Give the preparation type.
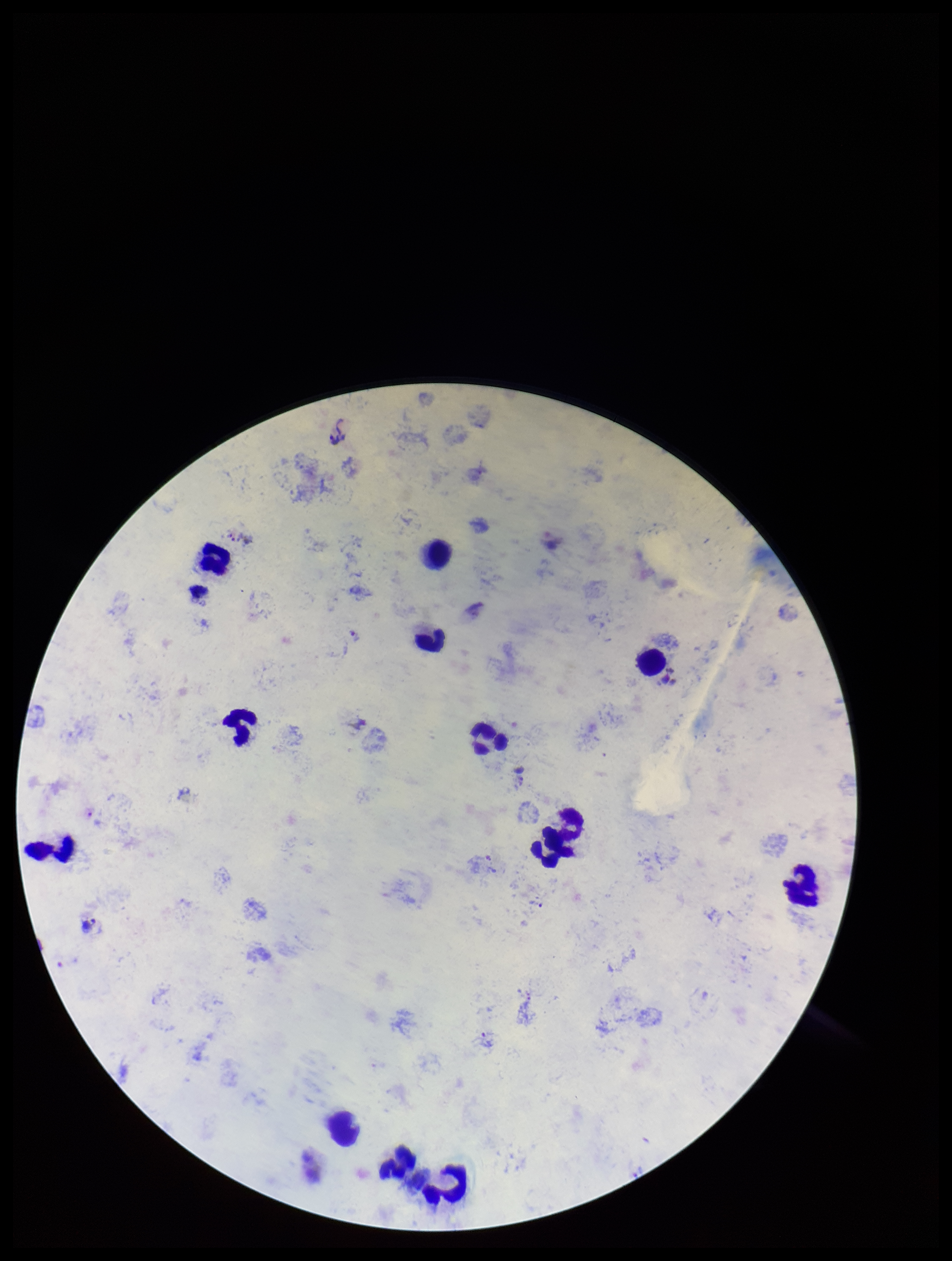
Thick.

Summary:
  - Species reported for this patient: Plasmodium vivax
  - Plasmodium parasites: seen
  - Stain: Giemsa
  - Leukocyte count: 12
  - Field of view: single
  - Patient malaria status: positive
  - Parasite count: 1
  - Capture: smartphone photograph through the microscope eyepiece
  - Image size: 952×1261 pixels